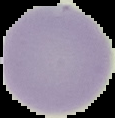
Summary:
  - Preparation: thin blood film
  - Image size: 115×118 pixels
  - Image type: segmented cell region on a black background
  - Result: negative for malaria parasites